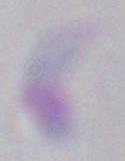

Summary:
  - Magnification: 1000x
  - Modality: photomicrograph
  - Identification: Toxoplasma gondii